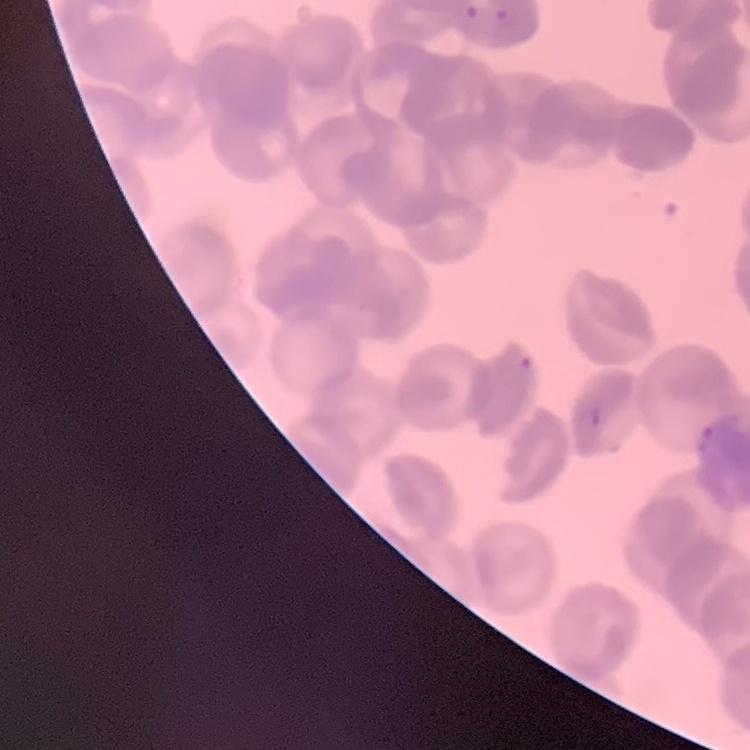

erythrocyte morphology = rouleaux formation
preparation = thin blood film
stain = Field's or Giemsa
image type = one tile cut from a larger photomicrograph